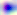

Summary:
  - Modality: micrograph
  - Identification: Toxoplasma gondii
  - Magnification: 400x